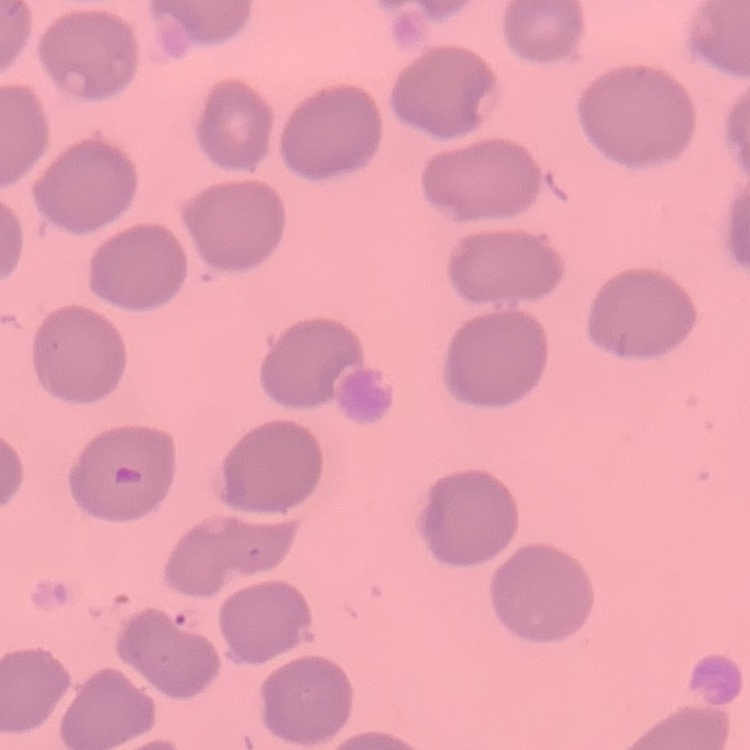
red blood cell morphology = no rouleaux formation
image type = square crop of a larger photomicrograph
stain = Field's or Giemsa
preparation = thin blood film